State the preparation type.
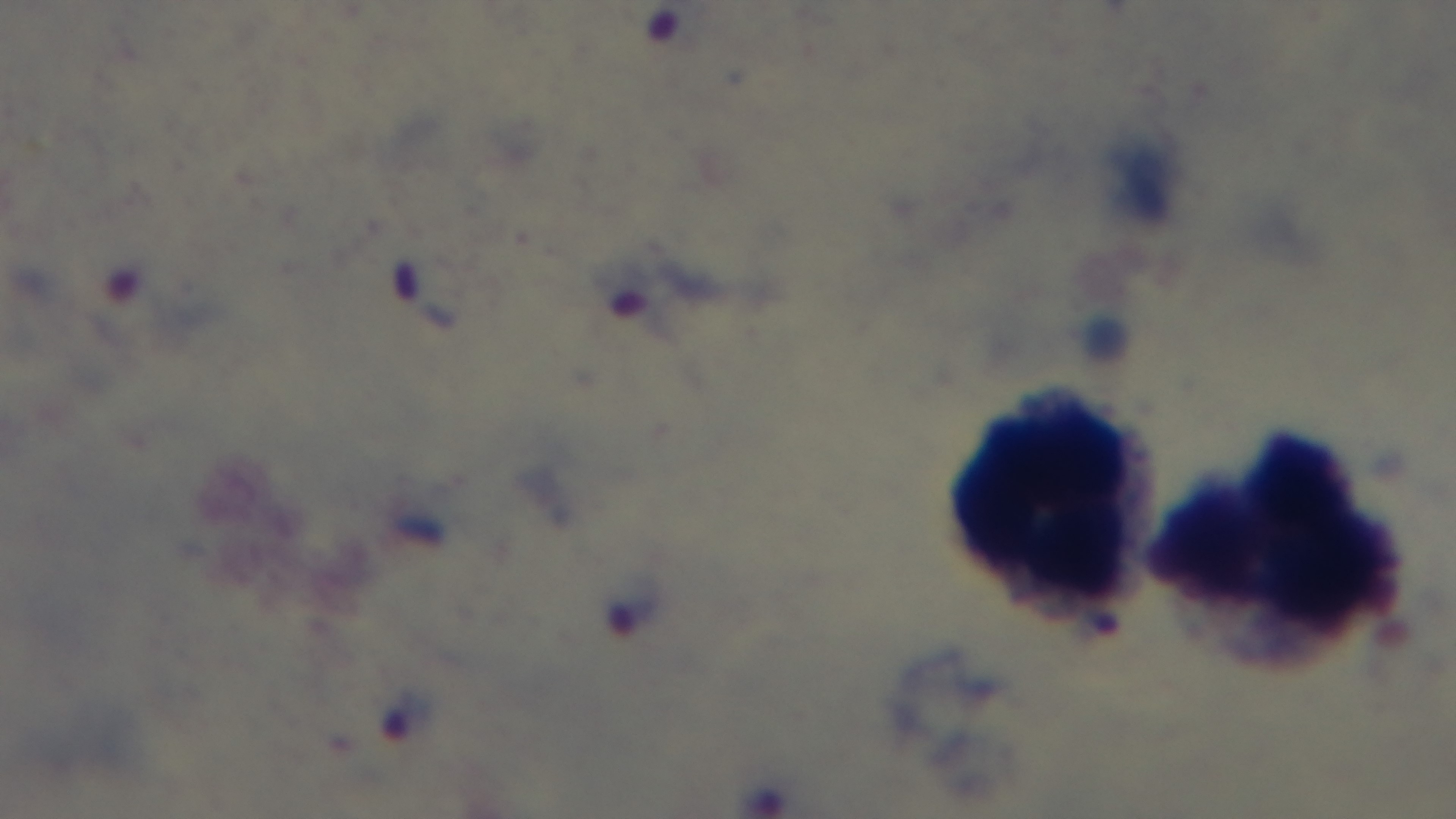
A thick smear.

capture = mounted 4K digital camera
stain = Giemsa
malaria status = infected
objective = 100x oil immersion
modality = light microscopy
field of view = single